Locate every malaria parasite.
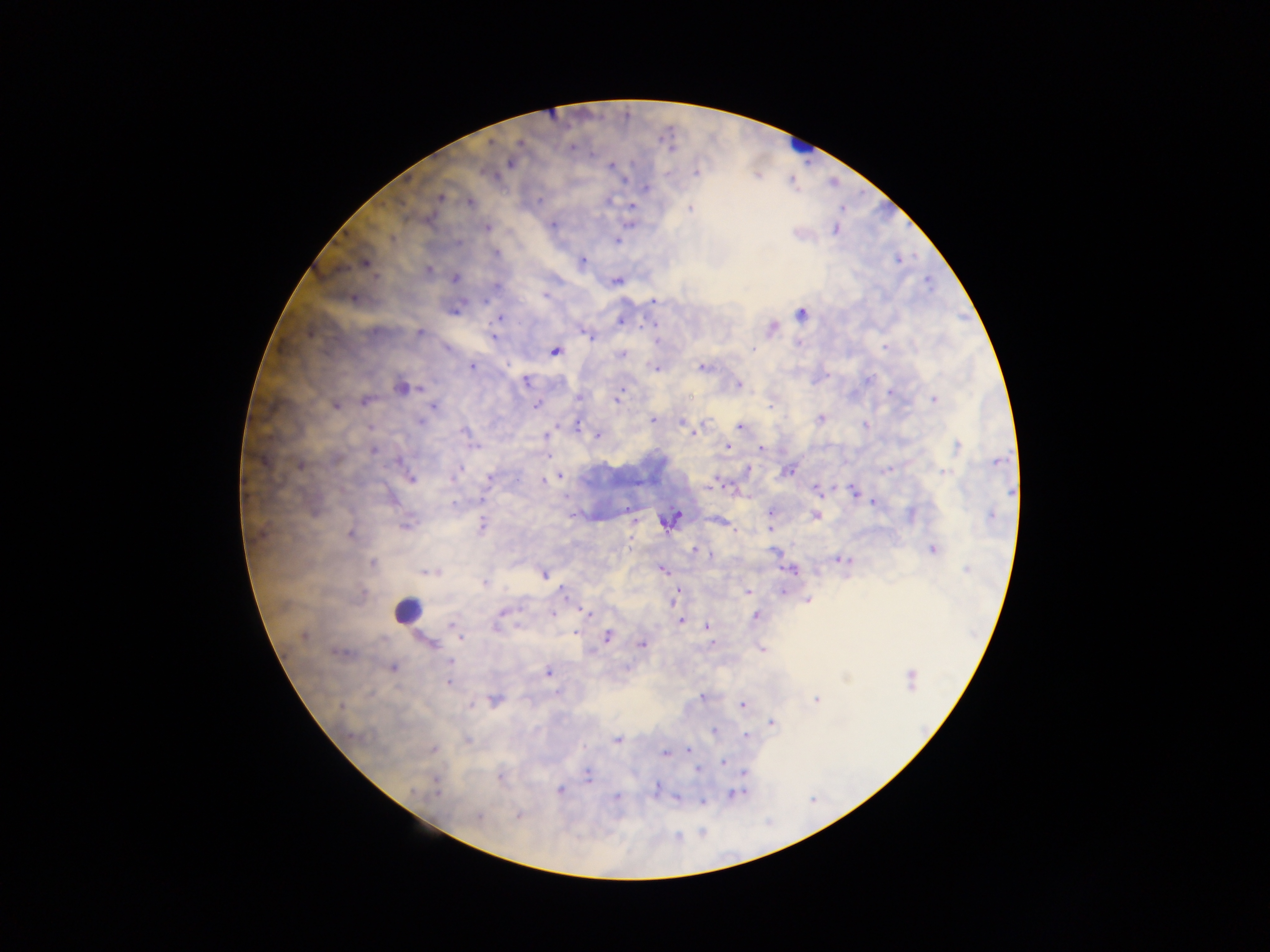

Approximate centers as x y in pixels.
Malaria parasites: 510 163; 611 166; 696 171; 439 196; 469 203; 631 206; 690 209; 488 227; 836 228; 616 241; 581 261; 364 263; 427 270; 455 278; 616 281; 352 298; 653 300; 801 313; 499 318; 620 320; 772 327; 420 332; 495 338; 555 351; 621 354; 472 366; 702 367; 655 368; 526 381; 737 384; 401 386; 891 391; 616 399; 933 399; 366 401; 335 405; 536 405; 433 406; 820 418; 653 419; 682 422; 741 426; 693 431; 546 434; 598 435; 726 446; 956 447; 374 449; 760 449; 300 464; 788 470; 560 476; 410 479; 544 480; 817 489; 855 493; 873 501; 454 503; 772 512; 911 514; 815 515; 671 519; 717 521; 405 525; 481 527; 770 528; 350 534; 932 550; 694 551; 842 559; 372 564; 793 569; 966 569; 663 570; 430 571; 543 573; 484 582; 781 589; 677 592; 748 592; 807 599; 553 613; 587 613; 502 615; 756 616; 681 621; 706 627; 303 635; 607 636; 460 637; 428 643; 641 643; 760 648; 340 652; 449 662; 392 667; 548 672; 910 679; 448 682; 816 699; 493 700; 743 704; 772 722; 745 735; 617 739; 466 740; 432 749; 687 751; 665 754; 723 761; 743 772; 587 775; 501 776; 655 789; 559 790; 734 794; 615 798; 678 798; 701 801; 518 815; 478 817.

leukocyte locations = approximate centers as x y in pixels: 799 145; 408 610
preparation = thick blood smear
field of view = single
capture = mobile-phone photograph through a microscope
country = Ghana
image size = 1270×952 pixels